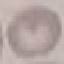
Malaria status: uninfected. Giemsa-stained preparation. Photographed with a smartphone camera at the microscope eyepiece. Thin blood film. Cell patch, automatically extracted from a larger field of view and resized to 64 × 64 pixels.